Identify the parasite.
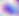

Toxoplasma gondii.

Summary:
  - Magnification: 400x
  - Modality: micrograph